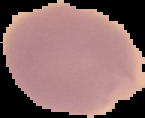

{
  "preparation": "thin blood film",
  "image_type": "segmented cell region with the area outside set to black",
  "image_size": "145×118 pixels",
  "malaria_status": "uninfected"
}